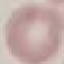
Summary:
  - Malaria status: uninfected
  - Stain: Giemsa
  - Preparation: thin blood smear
  - Image type: cell patch, automatically extracted from a larger field of view and resized to 64 × 64 pixels
  - Capture: smartphone through the microscope eyepiece